Report the malaria status of this cell.
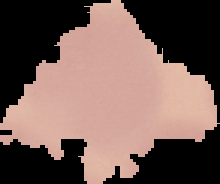

Uninfected.

From a thin blood film. Image is 220×184 pixels. Segmented cell region on a black background.